Assess this cell for malaria.
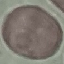

Uninfected.

image type = automatically extracted cell patch, resized to 64 × 64 pixels
capture = smartphone camera at the microscope eyepiece
stain = Giemsa
preparation = thin blood film